Describe the morphology of the erythrocytes.
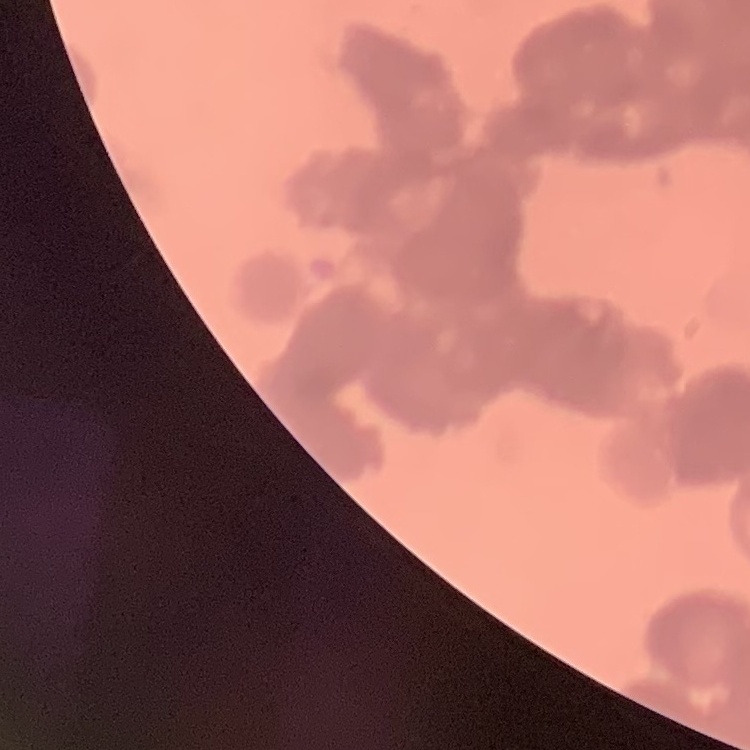
Rouleaux formation.

Square crop of a larger photomicrograph. Field's or Giemsa stain. Thin blood smear.